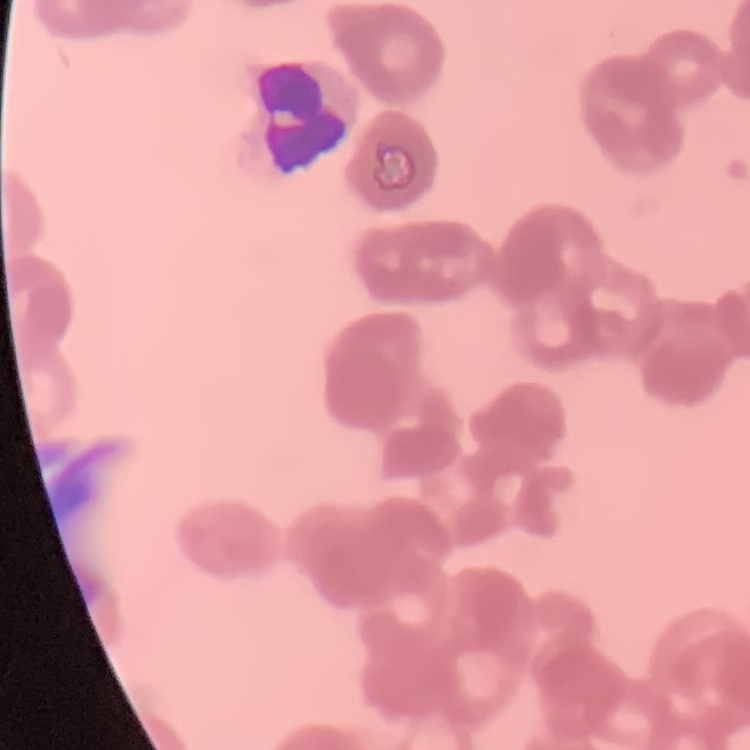
erythrocyte morphology = rouleaux formation
image type = one tile cut from a larger photomicrograph
preparation = thin blood smear
stain = Field's or Giemsa